Assess this cell for malaria.
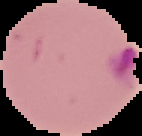

It is parasitized.

From a thin blood smear. Image is 142×136 pixels. Segmented cell region on a black background.